Classify this cell by malaria status.
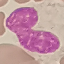
It is uninfected.

{
  "image_type": "cell patch, automatically extracted from a larger field of view and resized to 64 × 64 pixels",
  "capture": "smartphone camera at the microscope eyepiece",
  "preparation": "thin smear",
  "stain": "Giemsa"
}